Assess the morphology of the red blood cells.
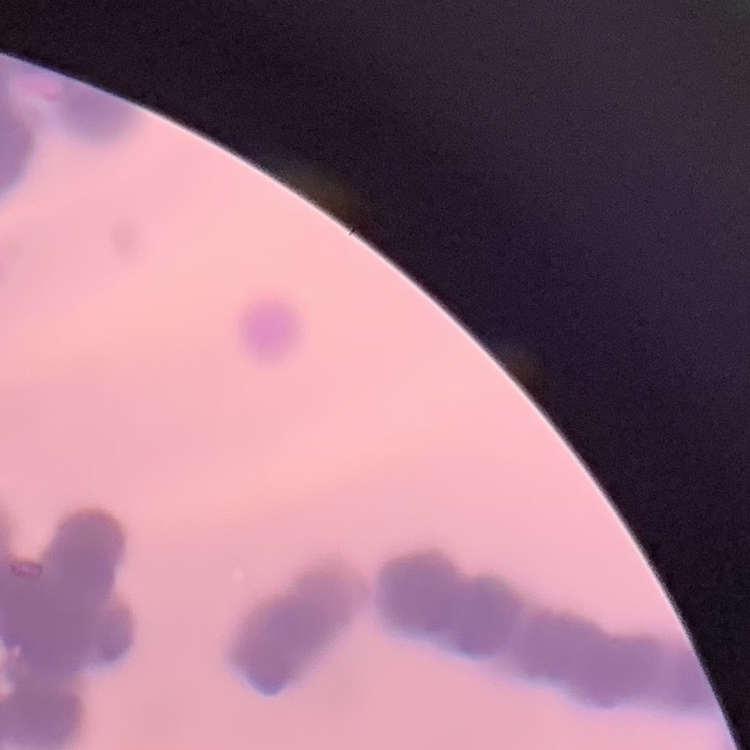
Rouleaux formation.

preparation: thin blood film
stain: Field's or Giemsa
image_type: square crop of a larger photomicrograph